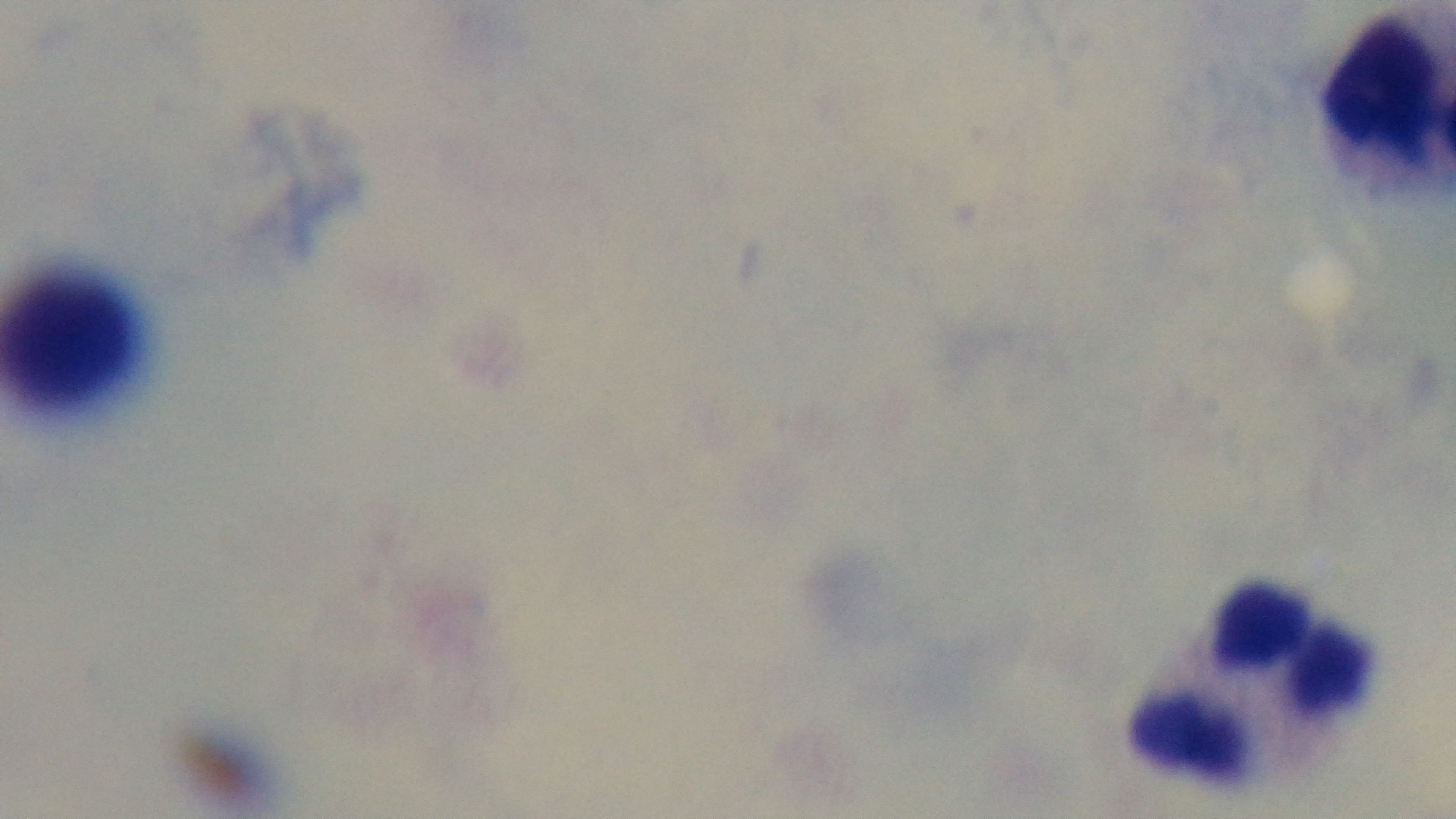

Giemsa-stained. Light microscopy. Mounted 4K digital camera. Preparation: thick smear. 100x oil-immersion objective. One field from the slide. Malaria status: negative.